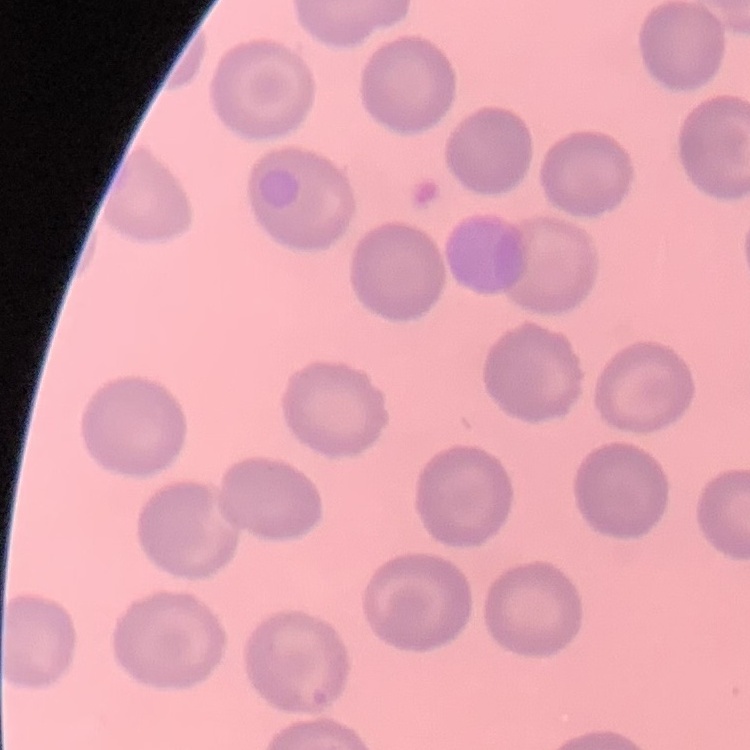
The red blood cells show no rouleaux formation. Stained with either Field's or Giemsa. Thin peripheral smear. Square crop of a larger photomicrograph.